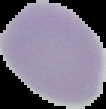
From a thin blood film. Image is 106×109 pixels. Malaria status: uninfected. Segmented cell region on a black background.